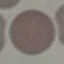 Result: no malaria parasites detected. Photographed with a smartphone camera at the microscope eyepiece. Giemsa stain. Thin blood film. Cell patch, automatically extracted from a larger field of view and resized to 64 × 64 pixels.